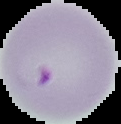

From a thin blood film. Cell region segmented out of the field of view; the surrounding area is masked to black. Malaria status: parasitized. Image is 121×124 pixels.